Identify the preparation type.
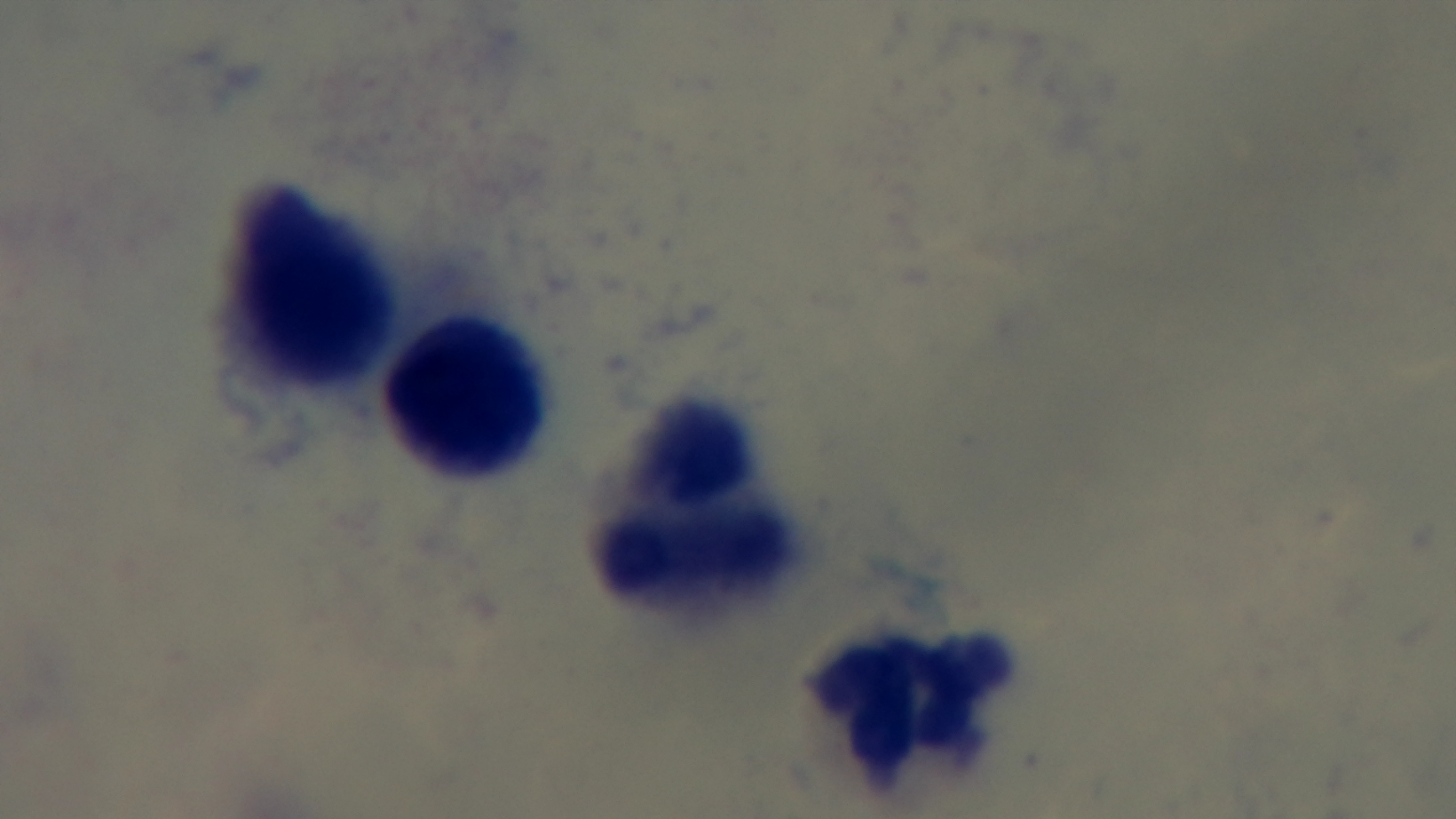
It is a thick blood film.

Summary:
  - Objective: 100x oil immersion
  - Field of view: one from the slide
  - Malaria status: uninfected
  - Capture: mounted 4K digital camera
  - Modality: light microscopy
  - Stain: Giemsa